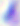
identification: Toxoplasma gondii
modality: micrograph
magnification: 400x